Assess the morphology of the erythrocytes.
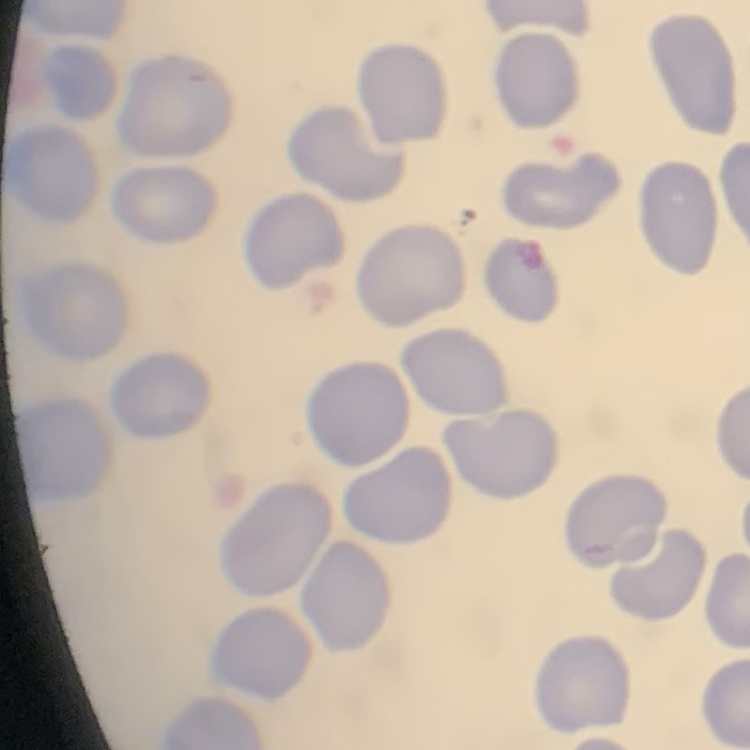

They show no rouleaux formation.

Stained with either Field's or Giemsa. Thin blood smear. One tile cut from a larger photomicrograph.